Name the parasite shown.
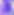

Toxoplasma gondii.

Photomicrograph. Captured at 400x magnification.